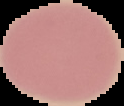
Segmented cell region on a black background. Malaria status: uninfected. Image is 124×106 pixels. From a thin blood smear.